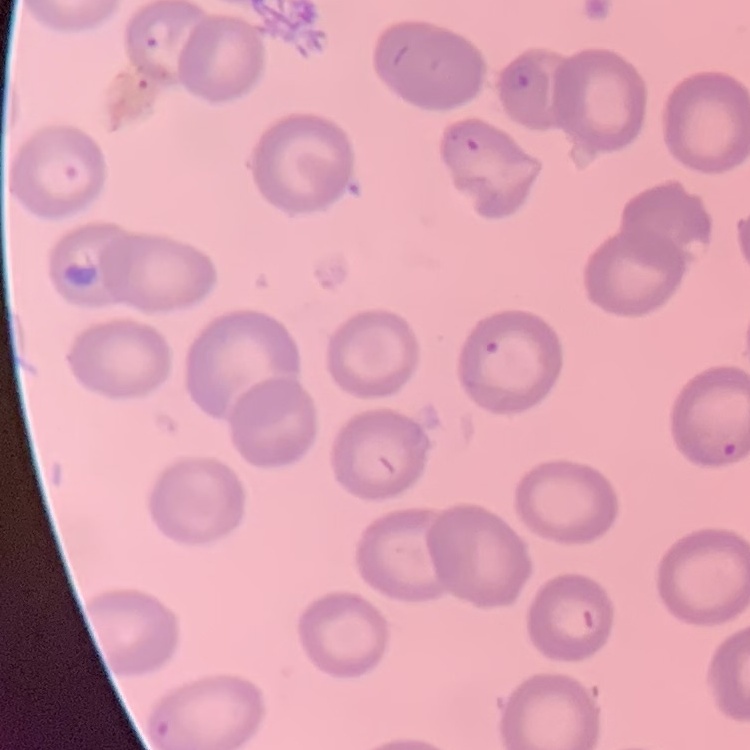
Summary:
  - Red blood cell morphology: no rouleaux formation
  - Preparation: thin blood film
  - Image type: one tile cut from a larger photomicrograph
  - Stain: Field's or Giemsa